Name the parasite shown.
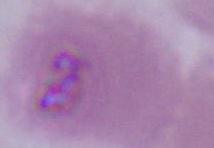

Plasmodium.

Photomicrograph. 400x or 1000x magnification.